Identify the preparation type.
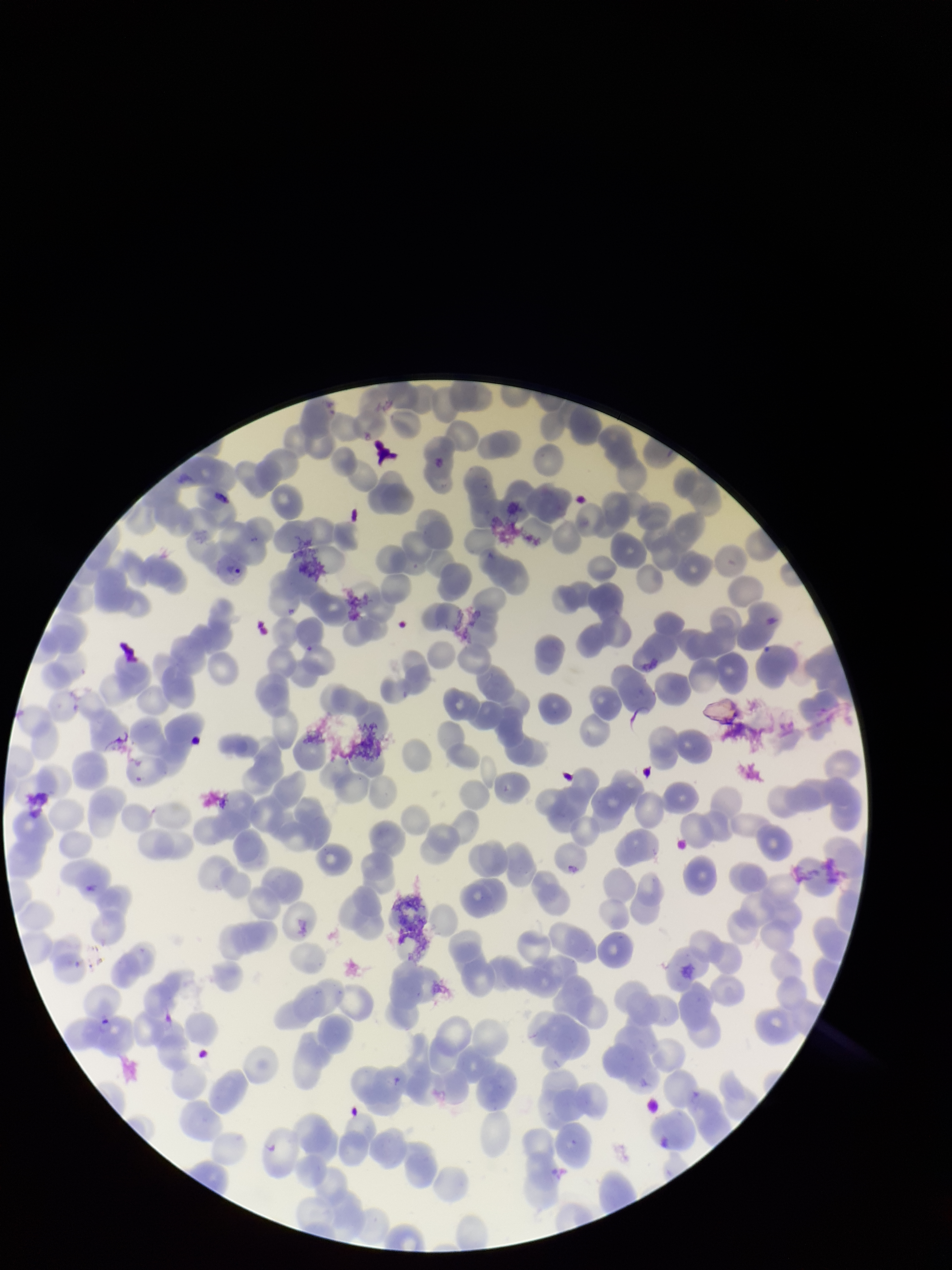
Thin.

patient malaria status = positive
stain = Giemsa
image size = 952×1270 pixels
red blood cell count = 196
species reported for this patient = Plasmodium falciparum
parasitized red blood cells = seen
capture = smartphone photograph through the microscope eyepiece
parasitized red blood cell count = 1
field of view = single